Report the malaria status of this cell.
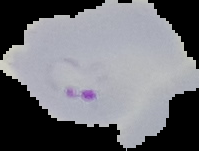

It is parasitized.

{
  "preparation": "thin blood smear",
  "image_type": "cell region segmented out of the field of view; surrounding area masked to black",
  "image_size": "199×151 pixels"
}